Name the parasite shown.
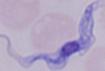
A trypanosome.

Summary:
  - Modality: micrograph
  - Magnification: 1000x